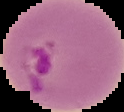 Result: Plasmodium parasites detected. Segmented cell region on a black background. From a thin blood film. Image is 124×112 pixels.